Identify the cell.
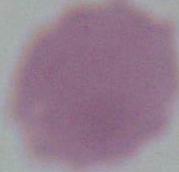
An erythrocyte.

Summary:
  - Magnification: 1000x
  - Modality: photomicrograph